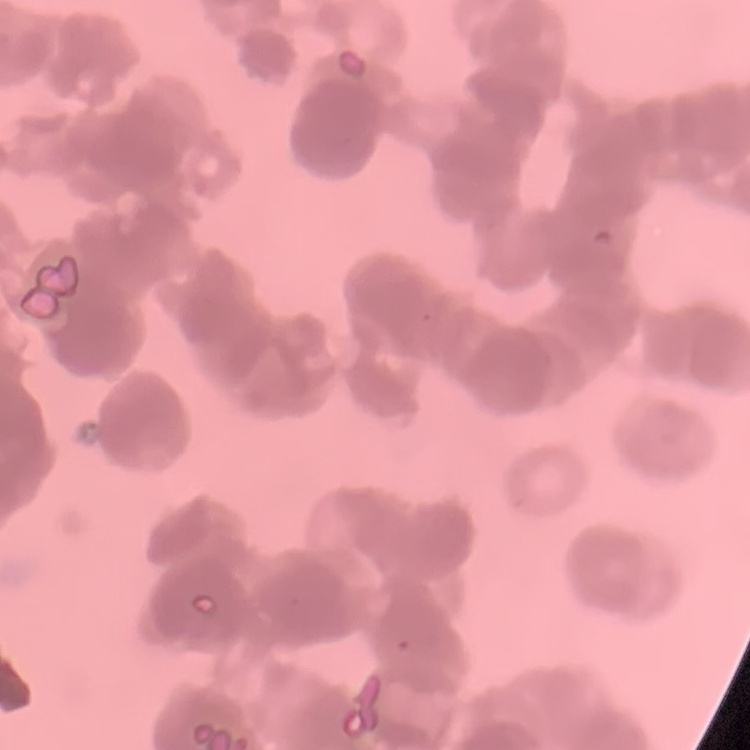

The red blood cells exhibit rouleaux formation. Stained with either Field's or Giemsa. Square crop of a larger photomicrograph. Thin peripheral smear.